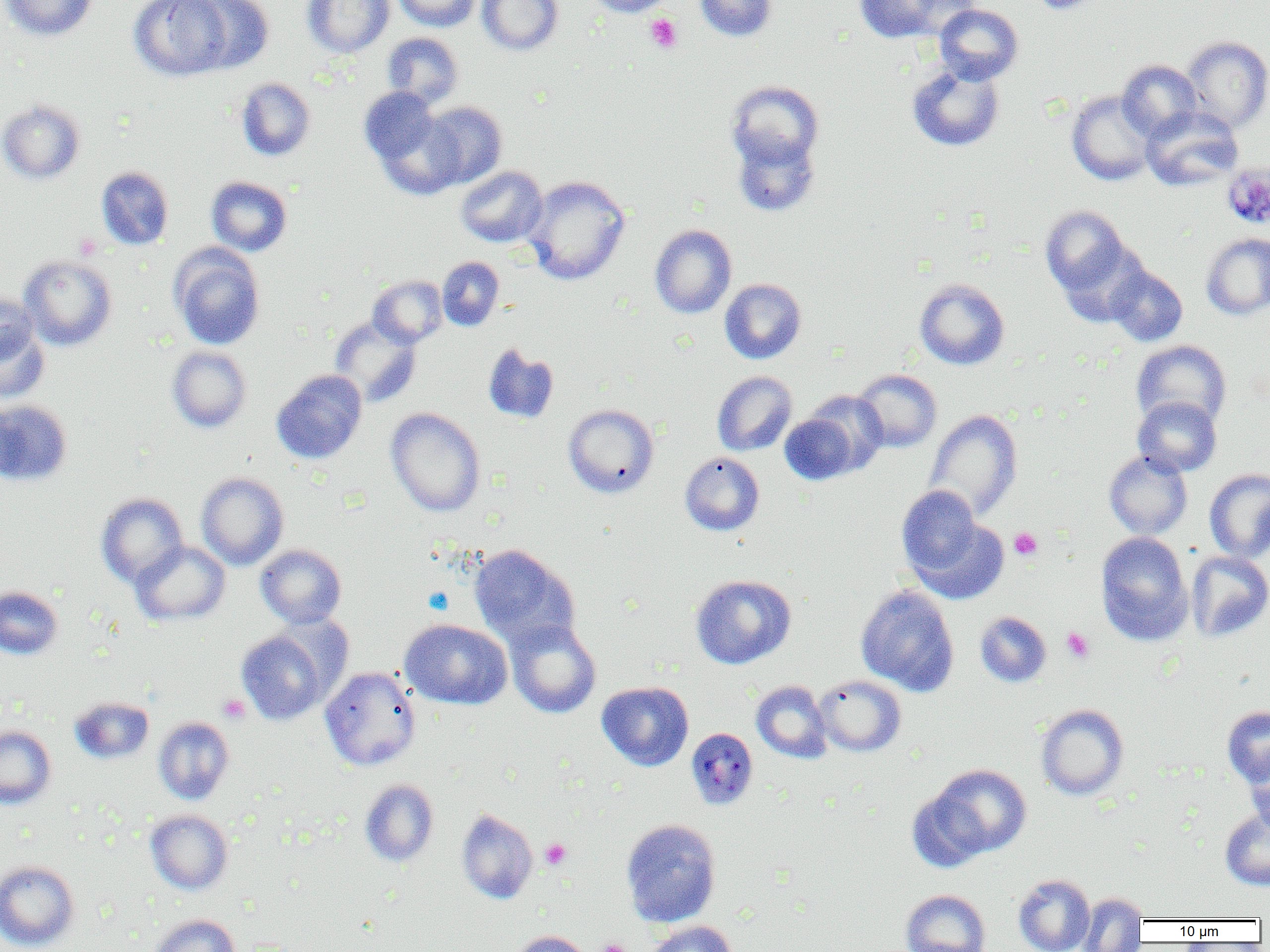
Summary:
  - Coordinate format: approximate bounding boxes as [x1, y1, x2, y2] in pixels
  - Platelet locations: [644, 14, 682, 53], [1009, 527, 1043, 561], [1061, 627, 1094, 662], [217, 694, 250, 723], [541, 839, 570, 869], [597, 938, 632, 952]
  - Uninfected red blood cell locations: [0, 0, 99, 41], [129, 0, 233, 81], [185, 0, 274, 74], [302, 0, 394, 58], [392, 0, 481, 32], [477, 0, 564, 55], [584, 0, 677, 17], [694, 0, 777, 42], [852, 0, 952, 44], [1029, 0, 1106, 14], [934, 4, 1023, 84], [381, 32, 464, 108], [1182, 35, 1270, 133], [1117, 59, 1202, 141], [907, 62, 1005, 152], [236, 77, 316, 162], [726, 80, 824, 171], [359, 87, 443, 170], [1066, 90, 1158, 185], [0, 99, 86, 184], [417, 101, 507, 190], [1141, 106, 1244, 191], [731, 130, 820, 217], [96, 166, 174, 250], [455, 166, 548, 247], [523, 175, 631, 285], [206, 176, 292, 256], [1040, 205, 1134, 301], [650, 224, 737, 318], [1201, 232, 1270, 320], [169, 245, 266, 350], [19, 254, 117, 351], [437, 256, 504, 331], [1106, 265, 1188, 346], [367, 275, 447, 347], [720, 278, 807, 364], [914, 278, 1010, 370], [0, 293, 40, 368], [0, 312, 50, 404], [329, 316, 422, 408], [1131, 340, 1232, 430], [483, 343, 559, 424], [166, 346, 252, 433], [271, 369, 368, 464], [853, 369, 942, 452], [711, 371, 797, 455], [804, 390, 888, 474], [1132, 396, 1222, 477], [0, 399, 72, 486], [562, 404, 660, 498], [385, 407, 486, 517], [924, 409, 1023, 522], [779, 414, 859, 486], [1104, 451, 1192, 539], [679, 452, 765, 535], [1204, 468, 1270, 563], [196, 472, 289, 570], [896, 485, 985, 580], [96, 493, 188, 587], [906, 511, 1008, 604], [1095, 531, 1193, 645], [131, 540, 230, 627], [255, 545, 347, 629], [469, 545, 580, 650], [1185, 551, 1270, 642], [690, 574, 796, 669], [855, 585, 960, 696], [0, 586, 63, 659], [975, 611, 1052, 687], [505, 618, 601, 719], [400, 619, 512, 709], [236, 627, 333, 725], [320, 666, 422, 771], [813, 675, 906, 756], [751, 680, 832, 763], [597, 681, 694, 771], [69, 696, 154, 764], [1035, 704, 1130, 800], [1222, 706, 1270, 788], [153, 716, 235, 805], [0, 725, 57, 810], [1244, 750, 1270, 833], [926, 764, 1032, 860], [359, 779, 439, 866], [1220, 808, 1270, 890], [145, 809, 233, 895], [457, 809, 538, 904], [621, 818, 722, 927], [0, 860, 80, 951], [1013, 873, 1095, 952], [900, 889, 990, 952], [1078, 893, 1147, 952], [149, 914, 239, 952], [645, 921, 738, 952], [508, 930, 591, 952]
  - Plasmodium malariae-infected red blood cell locations: [1222, 163, 1270, 229], [686, 728, 758, 810]
  - Slide-level diagnosis: Plasmodium malariae
  - Magnification: 1000x
  - Modality: light microscopy
  - Field of view: single
  - Preparation: thin blood smear
  - Image size: 1270×952 pixels